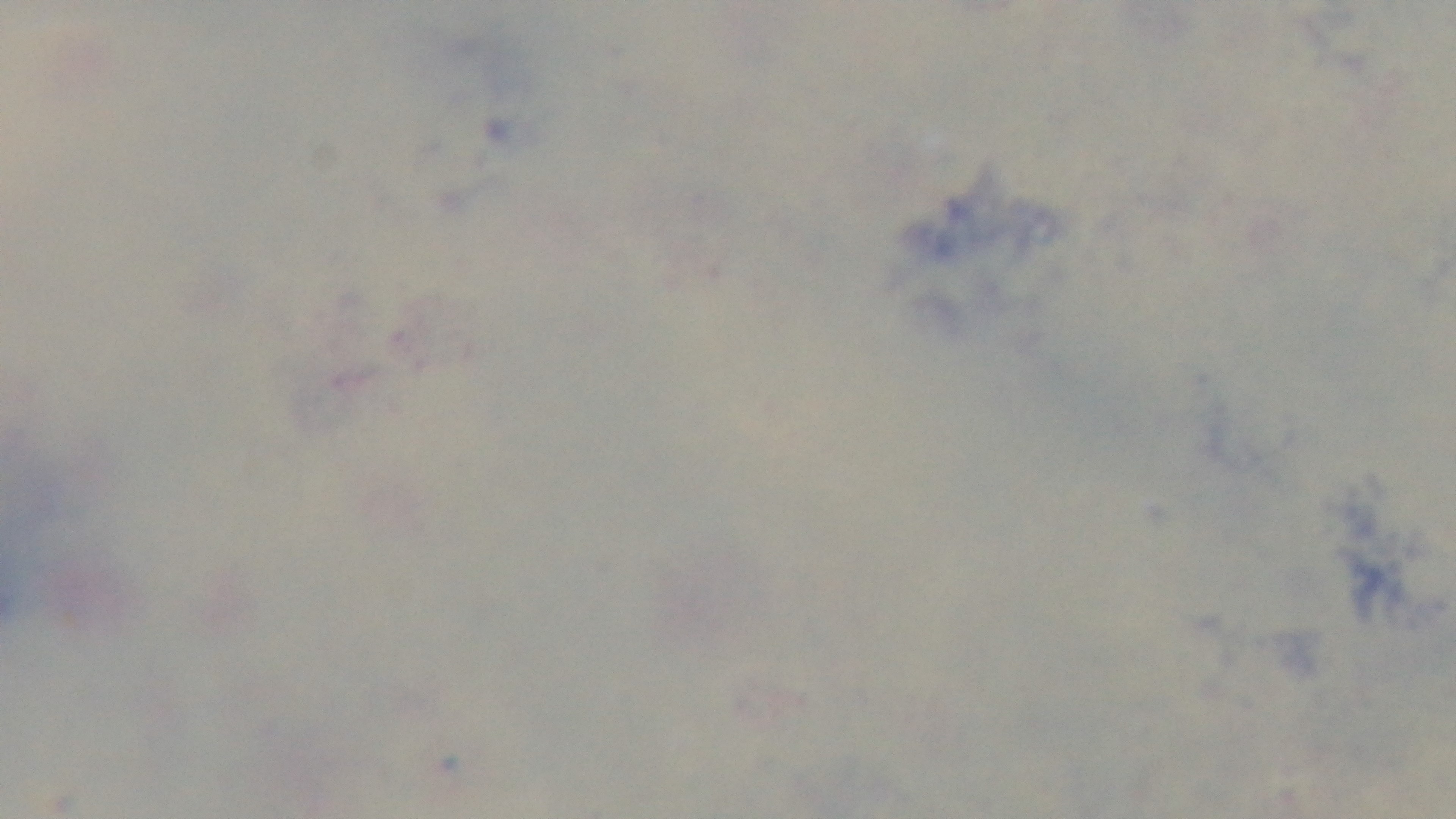 100x oil-immersion objective. Photomicrograph. Preparation: thick smear. Malaria status: negative. Mounted 4K digital camera. Giemsa stain. One field from the slide.